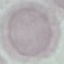

Result: no malaria parasites detected. Thin smear of blood. Acquired by smartphone through the microscope eyepiece. Cell patch, automatically extracted from a larger field of view and resized to 64 × 64 pixels. Giemsa stain.